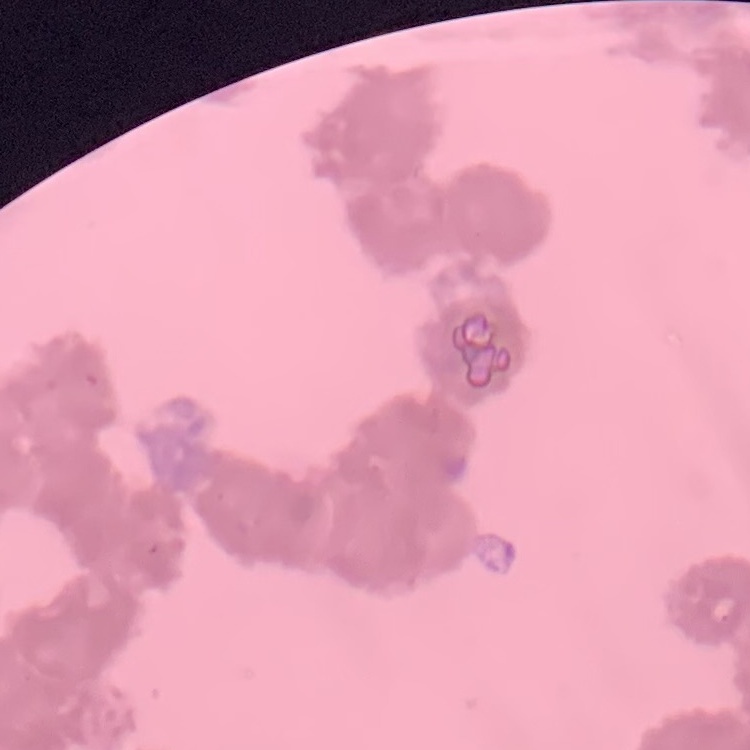
Summary:
  - Erythrocyte morphology: rouleaux formation
  - Preparation: thin peripheral smear
  - Stain: Field's or Giemsa
  - Image type: square crop of a larger photomicrograph